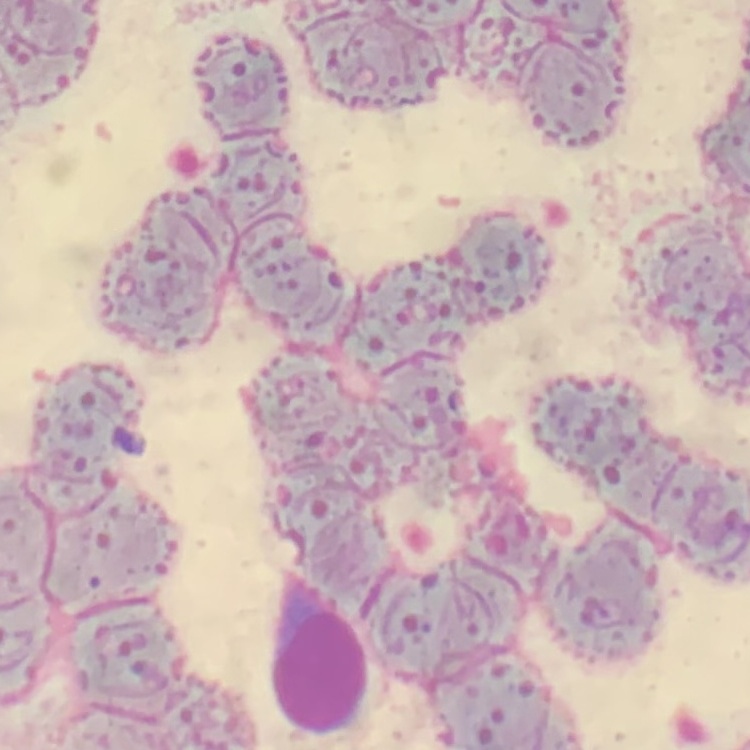
Summary:
  - Red blood cell morphology: rouleaux formation
  - Stain: Field's or Giemsa
  - Image type: square crop of a larger photomicrograph
  - Preparation: thin blood smear